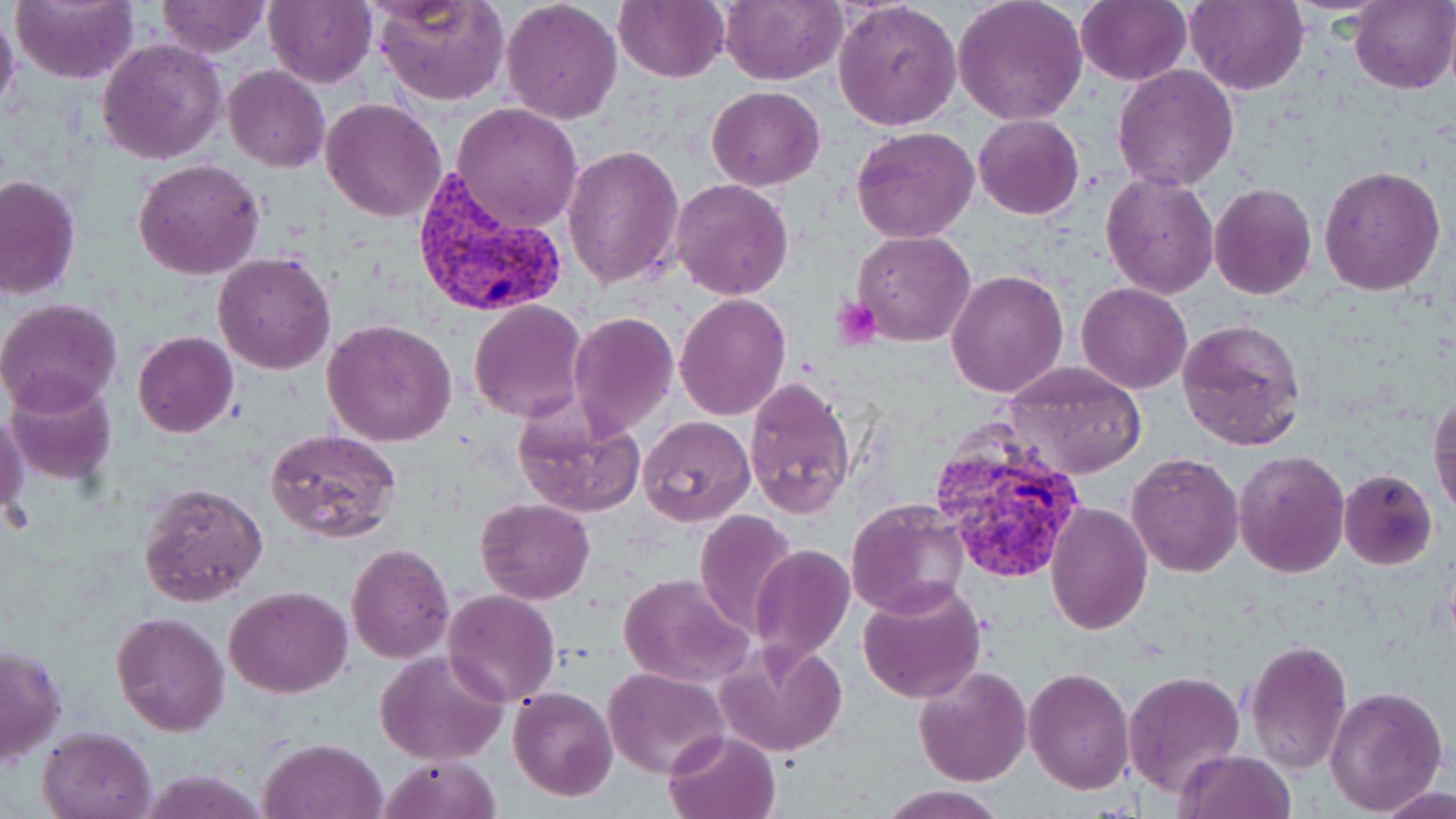
Approximate bounding boxes as named x1/y1/x2/y2 corners in pixels. Plasmodium vivax-infected red blood cell locations: (x1=409, y1=171, x2=570, y2=320), (x1=932, y1=416, x2=1091, y2=587). Uninfected red blood cell locations: (x1=11, y1=0, x2=139, y2=86), (x1=264, y1=0, x2=377, y2=88), (x1=372, y1=0, x2=511, y2=106), (x1=500, y1=0, x2=623, y2=124), (x1=721, y1=0, x2=844, y2=85), (x1=952, y1=0, x2=1089, y2=125), (x1=1077, y1=0, x2=1192, y2=86), (x1=156, y1=1, x2=269, y2=56), (x1=613, y1=1, x2=729, y2=83), (x1=832, y1=1, x2=963, y2=131), (x1=1184, y1=1, x2=1310, y2=96), (x1=1349, y1=1, x2=1455, y2=92), (x1=0, y1=6, x2=20, y2=119), (x1=98, y1=38, x2=227, y2=164), (x1=223, y1=65, x2=330, y2=172), (x1=1112, y1=65, x2=1239, y2=191), (x1=706, y1=85, x2=825, y2=191), (x1=322, y1=97, x2=449, y2=222), (x1=451, y1=102, x2=583, y2=232), (x1=972, y1=114, x2=1084, y2=219), (x1=851, y1=125, x2=980, y2=245), (x1=564, y1=145, x2=686, y2=291), (x1=133, y1=159, x2=264, y2=280), (x1=1318, y1=164, x2=1446, y2=296), (x1=1101, y1=172, x2=1218, y2=299), (x1=0, y1=174, x2=80, y2=301), (x1=671, y1=178, x2=795, y2=299), (x1=1208, y1=183, x2=1317, y2=300), (x1=852, y1=230, x2=977, y2=347), (x1=213, y1=251, x2=339, y2=375), (x1=946, y1=269, x2=1068, y2=397), (x1=1077, y1=283, x2=1192, y2=395), (x1=675, y1=294, x2=791, y2=421), (x1=0, y1=298, x2=125, y2=415), (x1=469, y1=300, x2=589, y2=422), (x1=568, y1=312, x2=679, y2=437), (x1=1177, y1=317, x2=1307, y2=452), (x1=322, y1=318, x2=459, y2=447), (x1=133, y1=332, x2=238, y2=438), (x1=1006, y1=359, x2=1149, y2=478), (x1=5, y1=373, x2=118, y2=485), (x1=745, y1=378, x2=856, y2=517), (x1=1430, y1=394, x2=1455, y2=519), (x1=513, y1=401, x2=646, y2=518), (x1=1, y1=409, x2=29, y2=528), (x1=637, y1=415, x2=755, y2=528), (x1=265, y1=428, x2=402, y2=543), (x1=1232, y1=448, x2=1350, y2=578), (x1=1126, y1=453, x2=1244, y2=577), (x1=1338, y1=469, x2=1439, y2=569), (x1=139, y1=481, x2=268, y2=607), (x1=475, y1=497, x2=595, y2=604), (x1=845, y1=497, x2=971, y2=620), (x1=1046, y1=503, x2=1152, y2=634), (x1=693, y1=508, x2=799, y2=637), (x1=346, y1=542, x2=455, y2=664), (x1=750, y1=543, x2=856, y2=667), (x1=617, y1=573, x2=753, y2=688), (x1=857, y1=578, x2=987, y2=704), (x1=224, y1=586, x2=352, y2=698), (x1=443, y1=589, x2=561, y2=706), (x1=110, y1=611, x2=230, y2=736), (x1=715, y1=636, x2=848, y2=759), (x1=1243, y1=639, x2=1352, y2=773), (x1=1, y1=641, x2=66, y2=765), (x1=376, y1=649, x2=510, y2=766), (x1=913, y1=665, x2=1033, y2=788), (x1=1024, y1=667, x2=1135, y2=795), (x1=603, y1=668, x2=730, y2=778), (x1=1123, y1=669, x2=1246, y2=796), (x1=1324, y1=683, x2=1449, y2=816), (x1=507, y1=687, x2=618, y2=801), (x1=37, y1=725, x2=156, y2=819), (x1=664, y1=727, x2=782, y2=819), (x1=258, y1=738, x2=388, y2=819), (x1=1175, y1=750, x2=1296, y2=819), (x1=377, y1=754, x2=503, y2=819), (x1=1376, y1=779, x2=1455, y2=819), (x1=877, y1=784, x2=1007, y2=819). Platelet locations: (x1=830, y1=296, x2=881, y2=350). Slide-level diagnosis: Plasmodium vivax. One field of a larger specimen. 1000x magnification. May-Grünwald-Giemsa-stained preparation. Image is 1456×819 pixels. Light microscopy. Thin blood film.